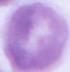

Micrograph. Captured at 1000x magnification. An erythrocyte is seen.